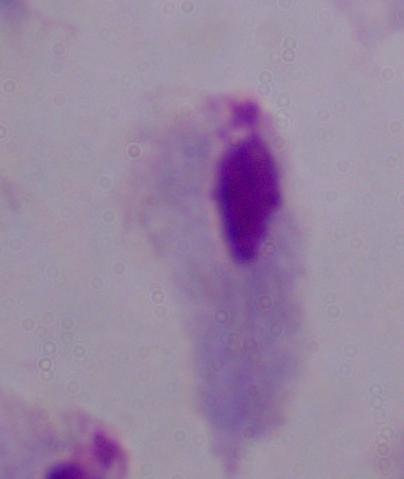
Photomicrograph. Captured at 1000x magnification. A trichomonad is seen.